Give the preparation type.
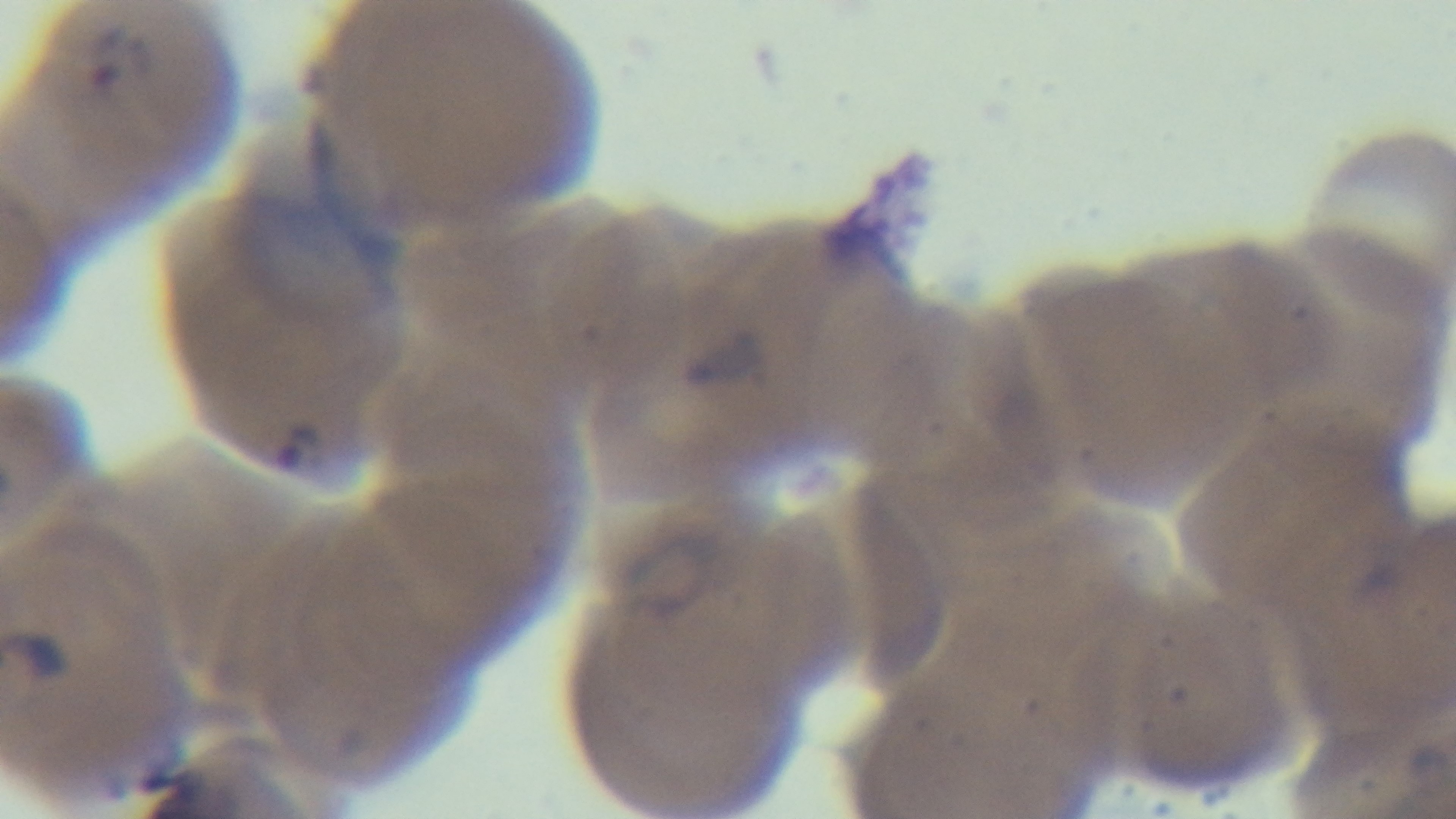

A thin smear.

{
  "modality": "light microscopy",
  "stain": "Giemsa",
  "capture": "mounted 4K digital camera",
  "objective": "100x oil immersion",
  "malaria_status": "infected",
  "field_of_view": "single"
}